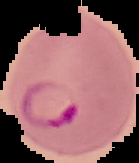
The area outside the segmented cell region is set to black. Image is 139×163 pixels. Malaria status: parasitized. From a thin blood film.